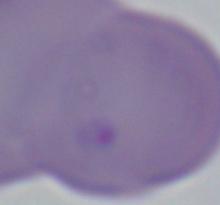
Summary:
  - Modality: photomicrograph
  - Magnification: 1000x
  - Identification: Babesia